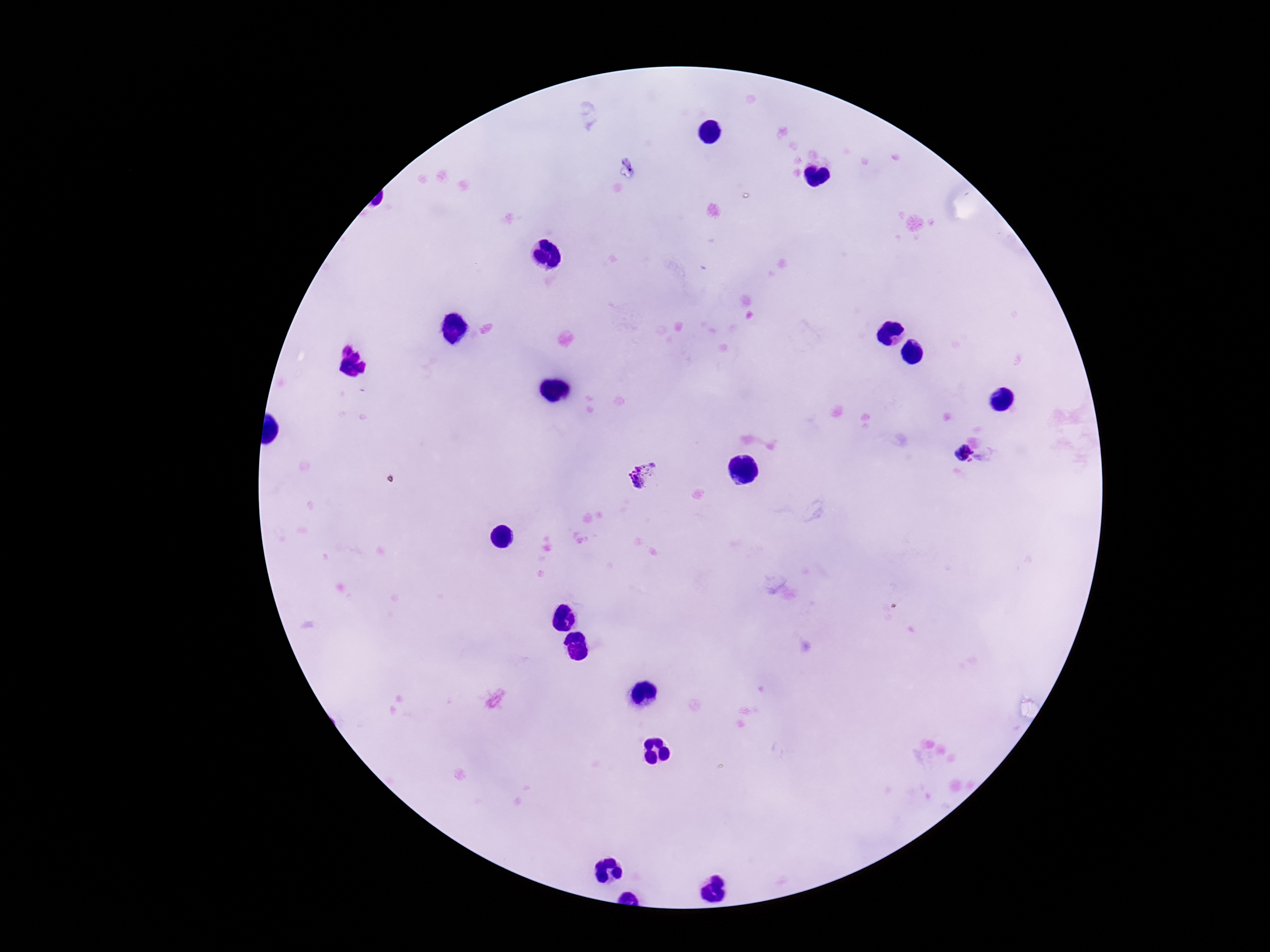

Approximate centers as [x, y] in pixels.
Summary:
  - Plasmodium parasite locations: [966, 454], [644, 476]
  - Patient malaria status: positive
  - Preparation: thick blood smear
  - Magnification: 100x
  - Field of view: single
  - Capture: smartphone camera through the microscope eyepiece
  - Image size: 1270×952 pixels
  - Stain: Giemsa